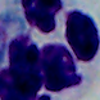
Micrograph. 1000x magnification. A leukocyte is shown.